Assess the morphology of the erythrocytes.
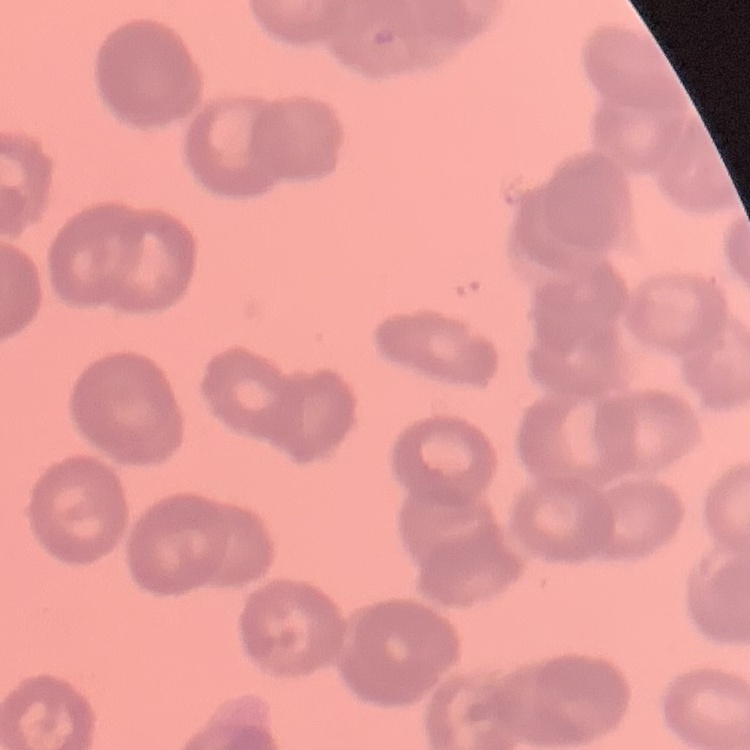

Rouleaux formation.

Summary:
  - Image type: one tile cut from a larger photomicrograph
  - Stain: Field's or Giemsa
  - Preparation: thin peripheral smear